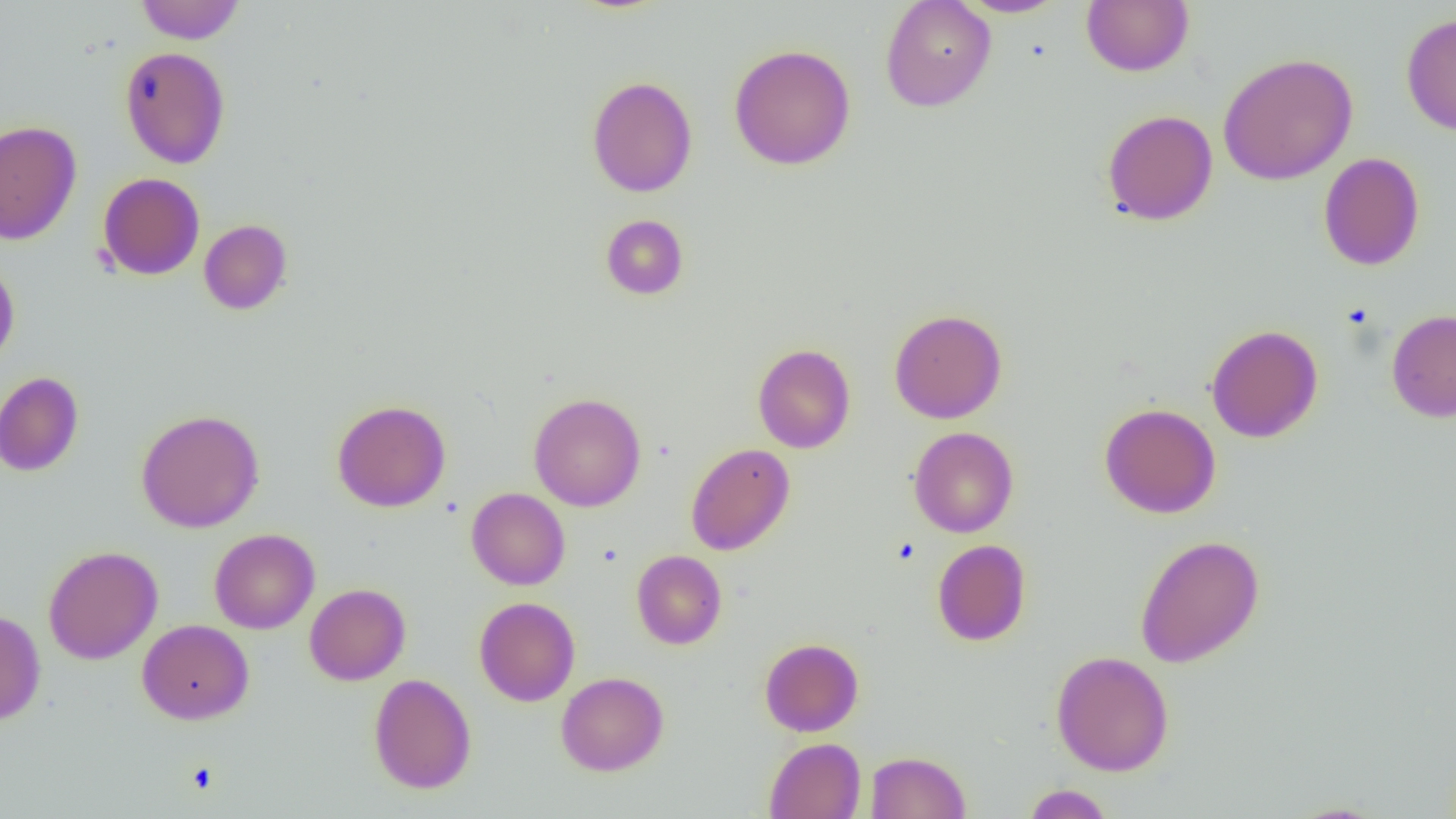

Summary:
  - Coordinate format: approximate bounding boxes as [x1, y1, x2, y2] in pixels
  - Uninfected red blood cell locations: [880, 0, 996, 112], [956, 0, 1069, 18], [1081, 0, 1194, 77], [136, 1, 245, 44], [1401, 13, 1456, 136], [729, 44, 856, 170], [119, 46, 230, 169], [1218, 52, 1358, 185], [586, 75, 698, 197], [1102, 109, 1218, 226], [0, 120, 82, 246], [1318, 152, 1424, 271], [97, 173, 205, 280], [600, 214, 689, 300], [199, 219, 293, 315], [0, 259, 20, 371], [889, 308, 1007, 423], [1386, 309, 1456, 423], [1206, 324, 1323, 443], [752, 343, 856, 453], [0, 372, 83, 476], [529, 393, 646, 512], [332, 399, 451, 512], [1100, 403, 1222, 518], [136, 408, 264, 533], [908, 427, 1019, 538], [685, 443, 795, 555], [466, 487, 570, 590], [209, 528, 320, 634], [1135, 534, 1265, 668], [932, 540, 1031, 646], [44, 545, 163, 664], [631, 550, 727, 649], [304, 583, 410, 685], [474, 597, 580, 706], [0, 610, 46, 726], [137, 619, 254, 724], [759, 638, 864, 736], [1050, 650, 1174, 776], [556, 672, 669, 775], [369, 673, 476, 794], [764, 738, 865, 819], [866, 751, 970, 818], [1022, 784, 1115, 818], [1283, 801, 1390, 818]
  - Slide-level diagnosis: negative for blood parasites
  - Modality: optical microscopy
  - Preparation: thin blood smear
  - Image size: 1456×819 pixels
  - Field of view: one of a larger specimen
  - Magnification: 1000x